Classify this cell by malaria status.
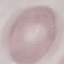

It is uninfected.

preparation = thin blood smear
capture = smartphone camera at the microscope eyepiece
image type = cell patch, automatically extracted from a larger field of view and resized to 64 × 64 pixels
stain = Giemsa